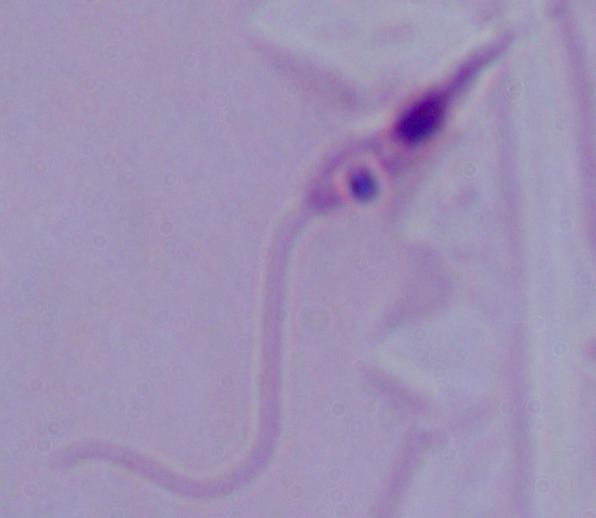
A Leishmania parasite is seen. Captured at 1000x magnification. Micrograph.